Give the position of every Plasmodium parasite.
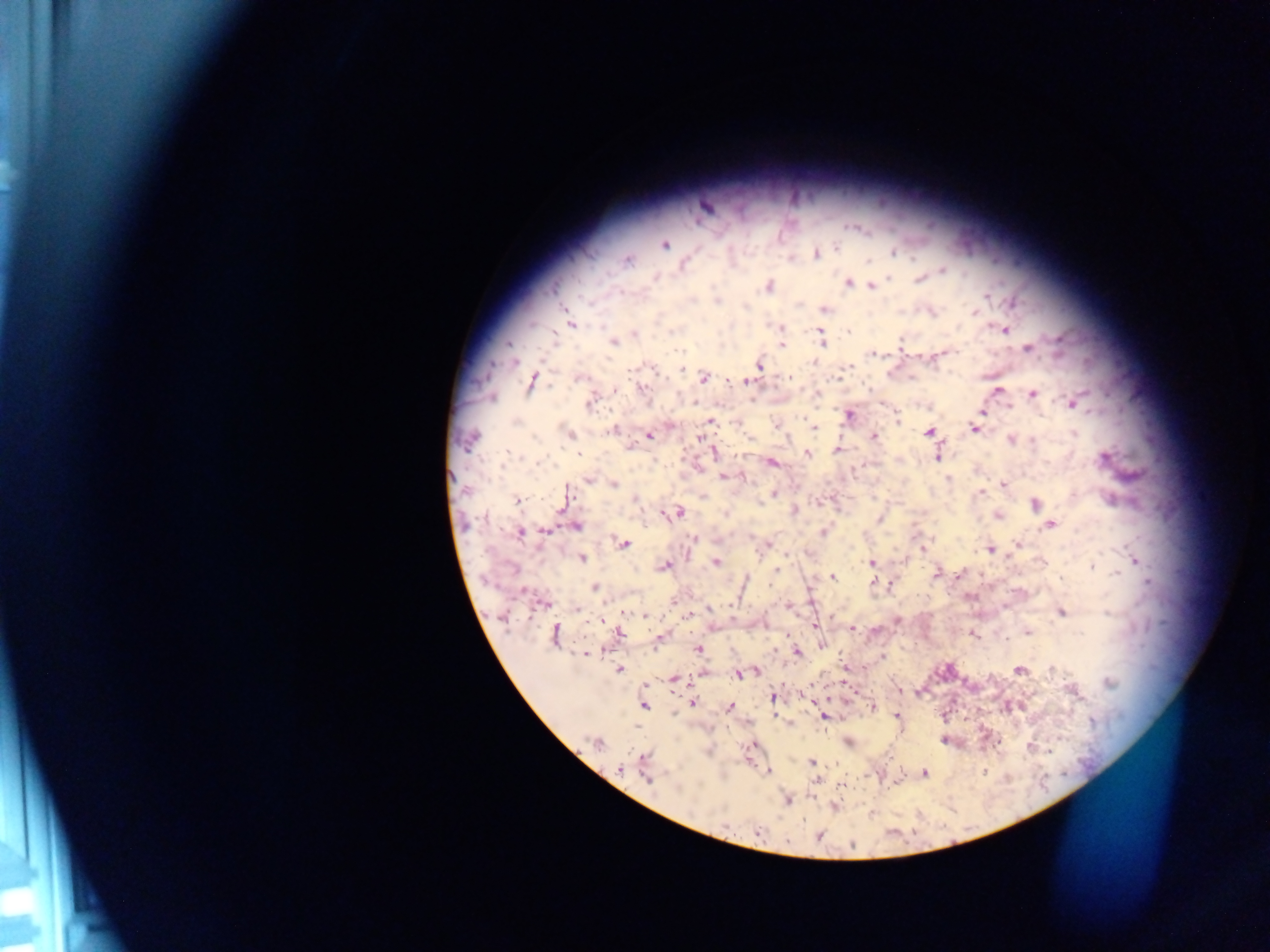

Approximate centers as [x, y] in pixels.
Plasmodium parasites: [665, 245], [836, 247], [893, 252], [816, 255], [867, 260], [627, 261], [684, 264], [943, 270], [655, 277], [920, 279], [848, 284], [767, 286], [872, 287], [718, 301], [1014, 302], [824, 310], [975, 312], [571, 324], [780, 327], [1004, 330], [848, 332], [634, 334], [822, 341], [613, 342], [509, 343], [900, 343], [781, 346], [1028, 349], [874, 354], [937, 357], [514, 362], [760, 365], [851, 367], [789, 377], [837, 377], [579, 378], [704, 378], [533, 381], [744, 381], [615, 389], [643, 389], [998, 389], [1033, 394], [589, 402], [1073, 403], [850, 414], [982, 414], [897, 421], [516, 422], [711, 422], [775, 425], [814, 428], [975, 428], [612, 429], [929, 432], [570, 433], [649, 435], [874, 437], [700, 439], [469, 440], [1012, 440], [631, 445], [838, 450], [715, 452], [807, 453], [508, 454], [579, 454], [937, 456], [1103, 458], [772, 463], [723, 476], [949, 478], [588, 479], [613, 484], [1003, 484], [567, 492], [981, 492], [773, 494], [517, 500], [635, 500], [1036, 504], [794, 510], [677, 512], [726, 514], [998, 516], [880, 519], [1050, 525], [576, 527], [545, 531], [824, 531], [521, 533], [694, 538], [624, 543], [1017, 545], [923, 550], [990, 550], [583, 559], [1135, 562], [716, 563], [871, 563], [665, 566], [1092, 567], [777, 570], [936, 573], [832, 576], [873, 583], [595, 587], [543, 604], [577, 609], [624, 612], [1062, 613], [646, 616], [688, 616], [600, 620], [815, 625], [853, 628], [1028, 632], [620, 634], [554, 635], [973, 635], [1005, 639], [698, 649], [797, 652], [585, 654], [619, 669], [1019, 670], [1053, 671], [757, 672], [739, 675], [673, 678], [1109, 683], [773, 697], [692, 703], [644, 705], [729, 707], [872, 707], [897, 715], [823, 716], [945, 740], [598, 744], [1030, 747], [644, 757], [811, 762], [620, 769], [768, 772], [923, 773], [648, 778], [788, 800], [758, 832], [819, 836], [788, 842], [852, 844].

Image is 1270×952 pixels. Thick blood film. Sample from Ghana. Single field of view. Photographed through a microscope with a mobile-phone camera.